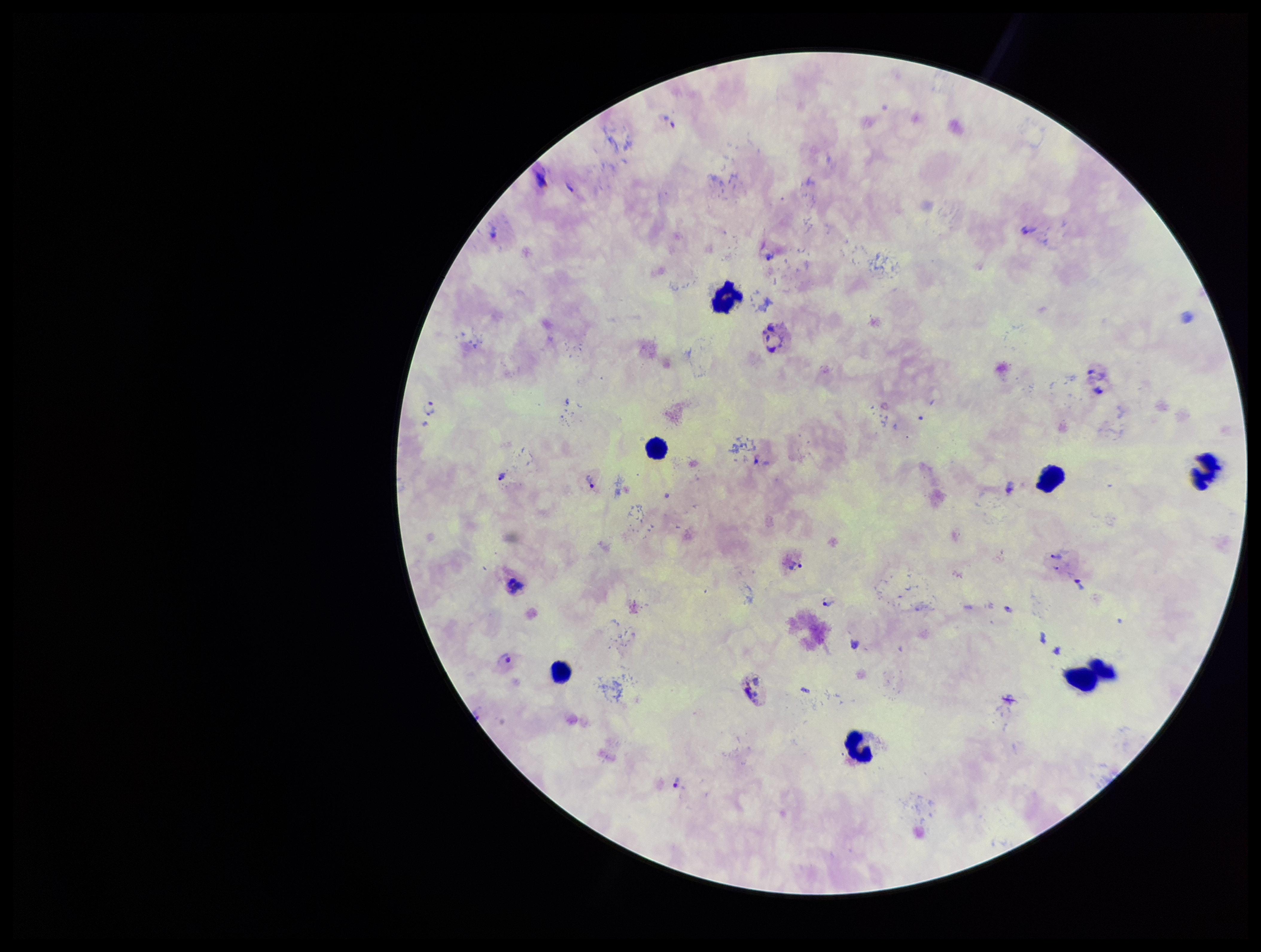
stain = Giemsa
parasite count = 11
field of view = single
Plasmodium parasites = seen
leukocyte count = 8
preparation = thick smear
capture = smartphone photograph through the microscope eyepiece
species reported for this patient = Plasmodium vivax
patient malaria status = infected
image size = 1261×952 pixels